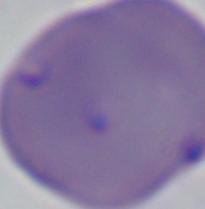

A Babesia parasite is shown. Captured at 1000x magnification. Photomicrograph.